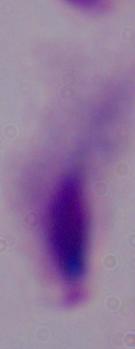
1000x magnification. Micrograph. A trichomonad is seen.